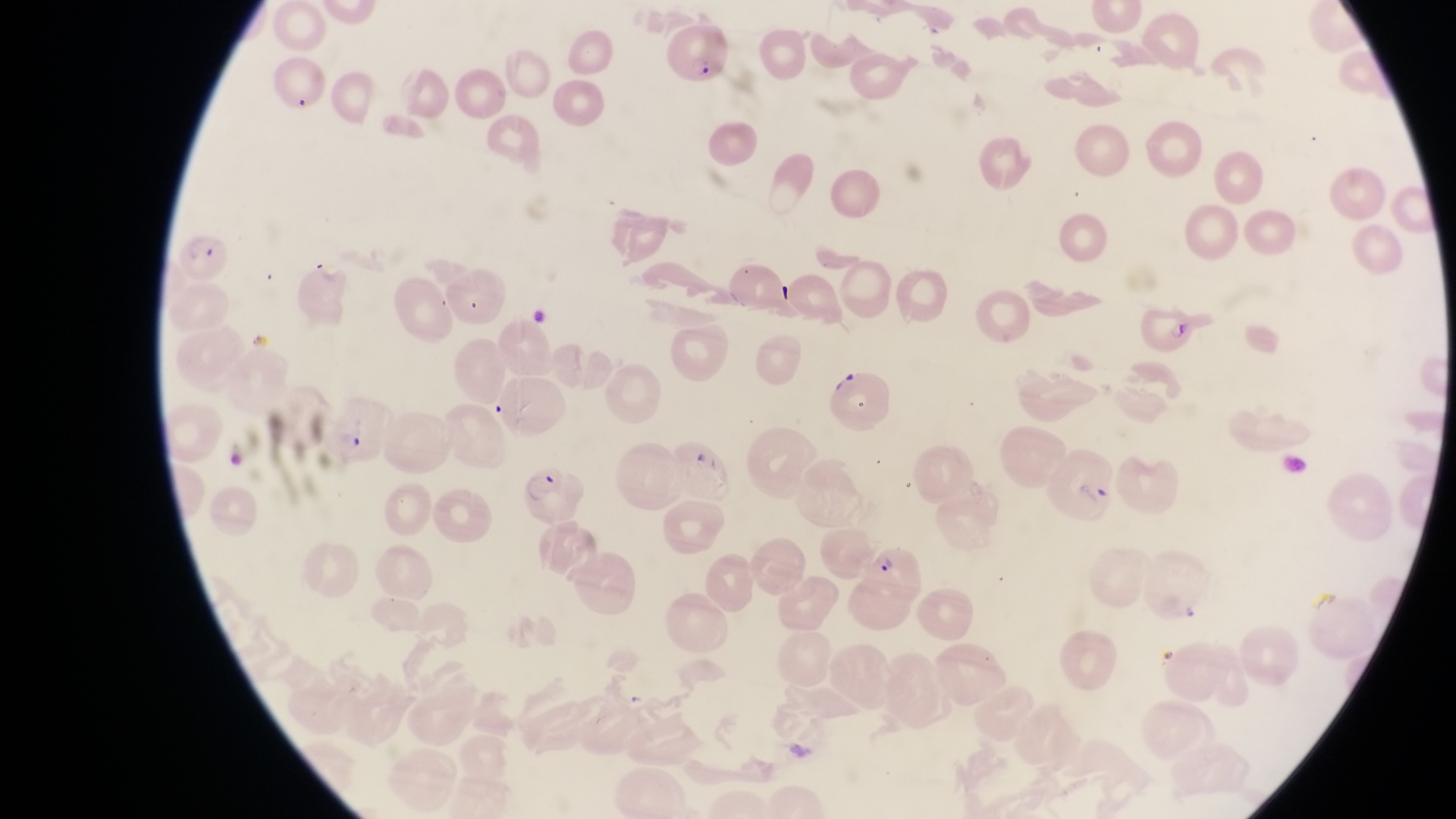
Approximate bounding boxes as (left, top, right, bottom) in pixels. Parasitised red blood cell locations: (663, 20, 732, 89), (182, 231, 234, 278), (1141, 306, 1197, 359), (831, 368, 890, 434), (329, 397, 387, 464), (1052, 447, 1116, 521), (522, 460, 588, 524), (861, 547, 925, 608). Single field of view. Thin blood smear. Magnification of 1000x. Photographed through the eyepiece of an Olympus CX-23 microscope with a smartphone camera. Image is 1456×819 pixels. Collected in Uganda.